Assess this cell for malaria.
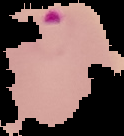

It is parasitized.

The area outside the segmented cell region is set to black. From a thin blood smear. Image is 124×136 pixels.